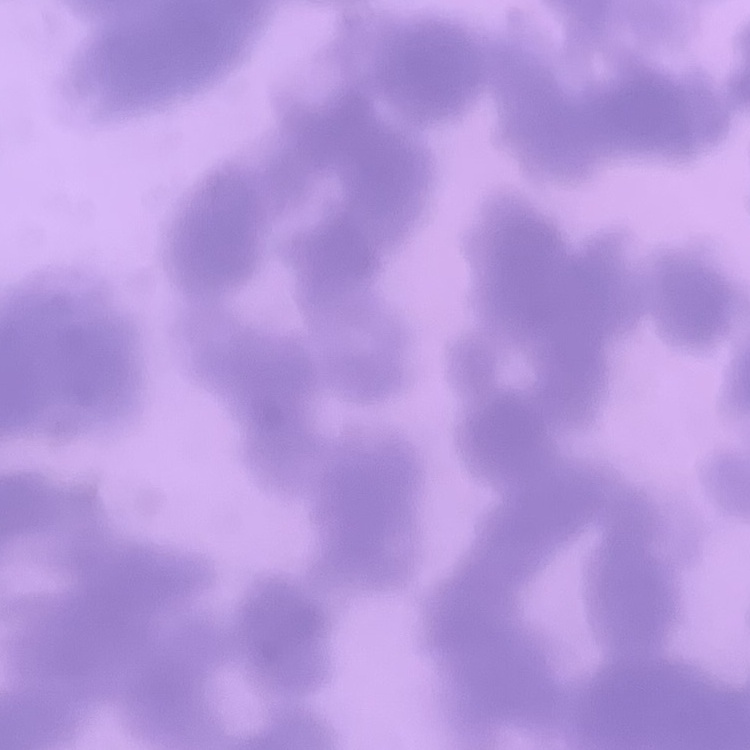
Summary:
  - Erythrocyte morphology: rouleaux formation
  - Stain: Field's or Giemsa
  - Image type: square crop of a larger photomicrograph
  - Preparation: thin blood smear